Name the blood parasite species.
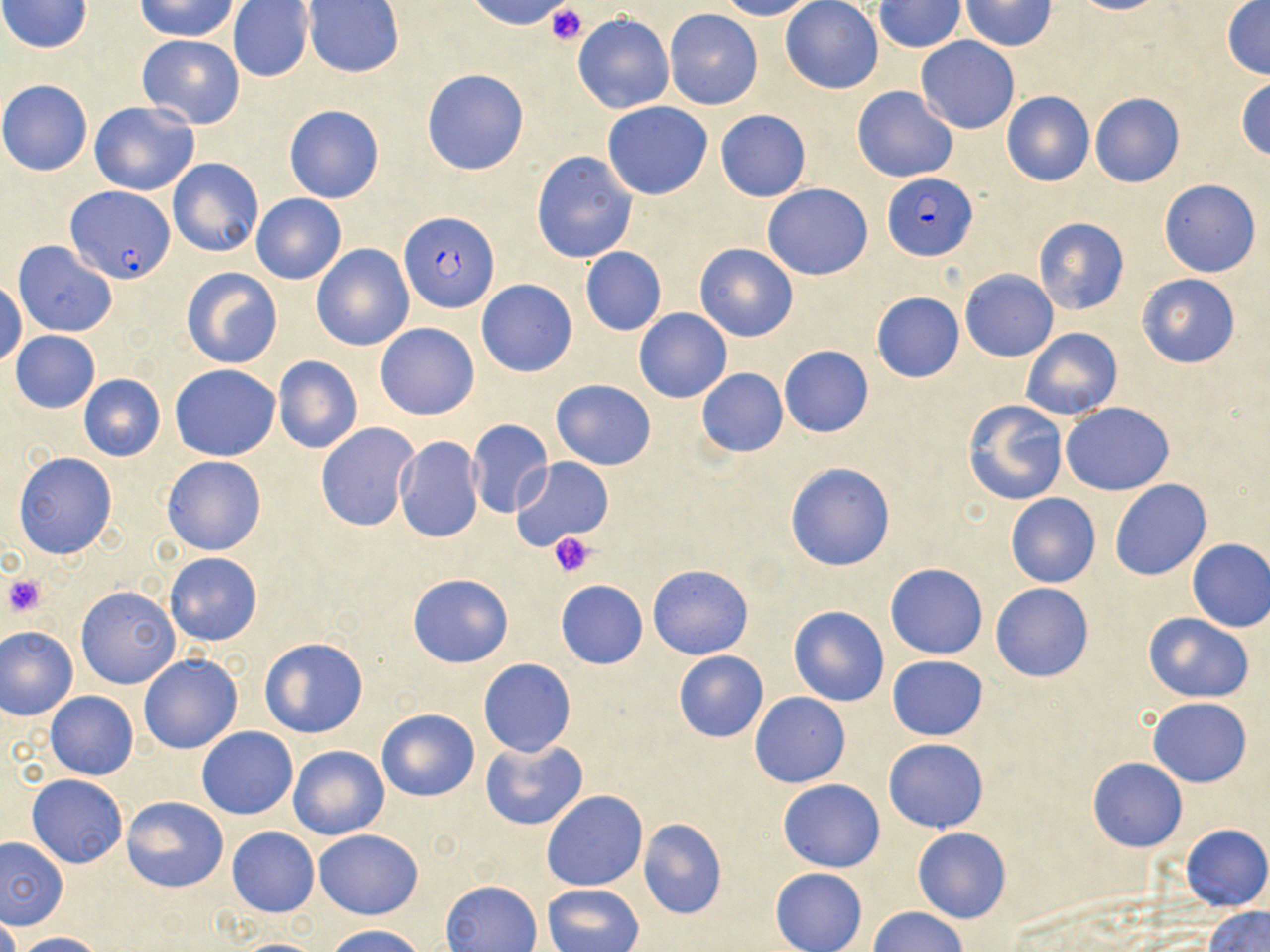
Plasmodium falciparum.

Summary:
  - Coordinate format: approximate bounding boxes as named x1/y1/x2/y2 corners in pixels
  - Platelet locations: (x1=545, y1=5, x2=590, y2=43), (x1=548, y1=530, x2=596, y2=578), (x1=3, y1=573, x2=48, y2=618)
  - Plasmodium falciparum-infected red blood cell locations: (x1=883, y1=173, x2=977, y2=260), (x1=68, y1=187, x2=174, y2=284), (x1=400, y1=211, x2=499, y2=314)
  - Uninfected red blood cell locations: (x1=2, y1=0, x2=93, y2=52), (x1=137, y1=0, x2=239, y2=41), (x1=466, y1=0, x2=577, y2=32), (x1=717, y1=0, x2=818, y2=21), (x1=781, y1=0, x2=883, y2=94), (x1=1068, y1=0, x2=1169, y2=15), (x1=1222, y1=0, x2=1270, y2=80), (x1=228, y1=1, x2=314, y2=84), (x1=304, y1=1, x2=404, y2=77), (x1=873, y1=1, x2=966, y2=53), (x1=960, y1=1, x2=1056, y2=50), (x1=664, y1=10, x2=763, y2=110), (x1=573, y1=13, x2=675, y2=113), (x1=138, y1=34, x2=245, y2=129), (x1=915, y1=36, x2=1020, y2=133), (x1=421, y1=69, x2=530, y2=176), (x1=1235, y1=77, x2=1270, y2=160), (x1=0, y1=79, x2=92, y2=175), (x1=852, y1=86, x2=959, y2=182), (x1=1001, y1=90, x2=1094, y2=186), (x1=1089, y1=92, x2=1186, y2=188), (x1=90, y1=101, x2=200, y2=195), (x1=602, y1=101, x2=713, y2=200), (x1=284, y1=105, x2=384, y2=203), (x1=715, y1=110, x2=811, y2=201), (x1=532, y1=151, x2=637, y2=264), (x1=167, y1=158, x2=265, y2=258), (x1=1159, y1=178, x2=1261, y2=278), (x1=762, y1=184, x2=873, y2=280), (x1=252, y1=194, x2=347, y2=284), (x1=1033, y1=216, x2=1129, y2=315), (x1=14, y1=241, x2=117, y2=337), (x1=694, y1=242, x2=800, y2=342), (x1=312, y1=244, x2=413, y2=351), (x1=580, y1=247, x2=666, y2=336), (x1=182, y1=268, x2=282, y2=368), (x1=960, y1=269, x2=1059, y2=361), (x1=1138, y1=273, x2=1240, y2=369), (x1=476, y1=280, x2=577, y2=377), (x1=0, y1=281, x2=26, y2=368), (x1=871, y1=292, x2=964, y2=383), (x1=634, y1=308, x2=732, y2=403), (x1=375, y1=323, x2=479, y2=420), (x1=1020, y1=328, x2=1121, y2=421), (x1=10, y1=330, x2=101, y2=413), (x1=779, y1=345, x2=873, y2=438), (x1=273, y1=355, x2=363, y2=454), (x1=696, y1=359, x2=875, y2=447), (x1=170, y1=365, x2=280, y2=460), (x1=696, y1=368, x2=788, y2=457), (x1=79, y1=374, x2=166, y2=461), (x1=551, y1=380, x2=657, y2=469), (x1=961, y1=398, x2=1069, y2=506), (x1=1060, y1=401, x2=1175, y2=495), (x1=467, y1=419, x2=553, y2=518), (x1=317, y1=422, x2=419, y2=531), (x1=395, y1=436, x2=484, y2=542), (x1=13, y1=452, x2=117, y2=558), (x1=162, y1=455, x2=267, y2=556), (x1=511, y1=457, x2=613, y2=550), (x1=785, y1=461, x2=896, y2=571), (x1=1109, y1=479, x2=1212, y2=581), (x1=1005, y1=493, x2=1101, y2=588), (x1=1185, y1=538, x2=1270, y2=633), (x1=165, y1=553, x2=262, y2=646), (x1=886, y1=563, x2=988, y2=659), (x1=648, y1=564, x2=753, y2=660), (x1=409, y1=574, x2=512, y2=668), (x1=555, y1=580, x2=648, y2=669), (x1=990, y1=582, x2=1094, y2=682), (x1=75, y1=585, x2=180, y2=689), (x1=788, y1=606, x2=888, y2=707), (x1=1142, y1=613, x2=1255, y2=704), (x1=1, y1=626, x2=79, y2=719), (x1=258, y1=636, x2=369, y2=738), (x1=672, y1=649, x2=769, y2=743), (x1=139, y1=653, x2=243, y2=755), (x1=887, y1=655, x2=987, y2=740), (x1=478, y1=659, x2=577, y2=758), (x1=45, y1=690, x2=139, y2=780), (x1=750, y1=692, x2=849, y2=788), (x1=1148, y1=697, x2=1253, y2=786), (x1=376, y1=708, x2=479, y2=801), (x1=197, y1=725, x2=298, y2=819), (x1=480, y1=739, x2=588, y2=832), (x1=884, y1=739, x2=989, y2=833), (x1=288, y1=745, x2=390, y2=840), (x1=1087, y1=757, x2=1188, y2=852), (x1=27, y1=775, x2=128, y2=868), (x1=779, y1=779, x2=885, y2=872), (x1=542, y1=790, x2=648, y2=892), (x1=122, y1=796, x2=228, y2=892), (x1=637, y1=817, x2=727, y2=920), (x1=1182, y1=825, x2=1268, y2=912), (x1=227, y1=827, x2=318, y2=918), (x1=912, y1=828, x2=1011, y2=923), (x1=313, y1=829, x2=423, y2=920), (x1=0, y1=836, x2=67, y2=930), (x1=770, y1=867, x2=867, y2=952), (x1=442, y1=880, x2=541, y2=952), (x1=542, y1=883, x2=644, y2=951), (x1=1203, y1=905, x2=1270, y2=952), (x1=869, y1=906, x2=967, y2=952), (x1=0, y1=909, x2=20, y2=952), (x1=325, y1=925, x2=428, y2=952), (x1=14, y1=931, x2=109, y2=952), (x1=227, y1=937, x2=333, y2=951)
  - Image size: 1270×952 pixels
  - Field of view: single
  - Modality: light microscopy
  - Preparation: thin blood smear
  - Stain: May-Grünwald-Giemsa
  - Magnification: 1000x